Assess this cell for malaria.
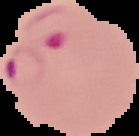

Parasitized.

image_size: 139×136 pixels
preparation: thin blood film
image_type: segmented cell region with the area outside set to black